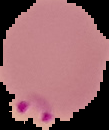
{
  "image_type": "segmented cell region with the area outside set to black",
  "malaria_status": "parasitized",
  "preparation": "thin blood film",
  "image_size": "109×130 pixels"
}